Identify the parasite.
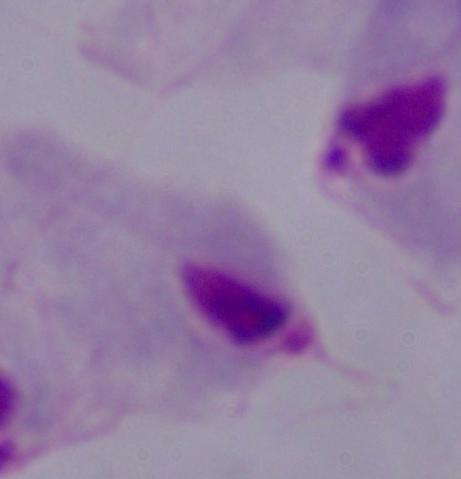
This is a trichomonad.

1000x magnification. Micrograph.